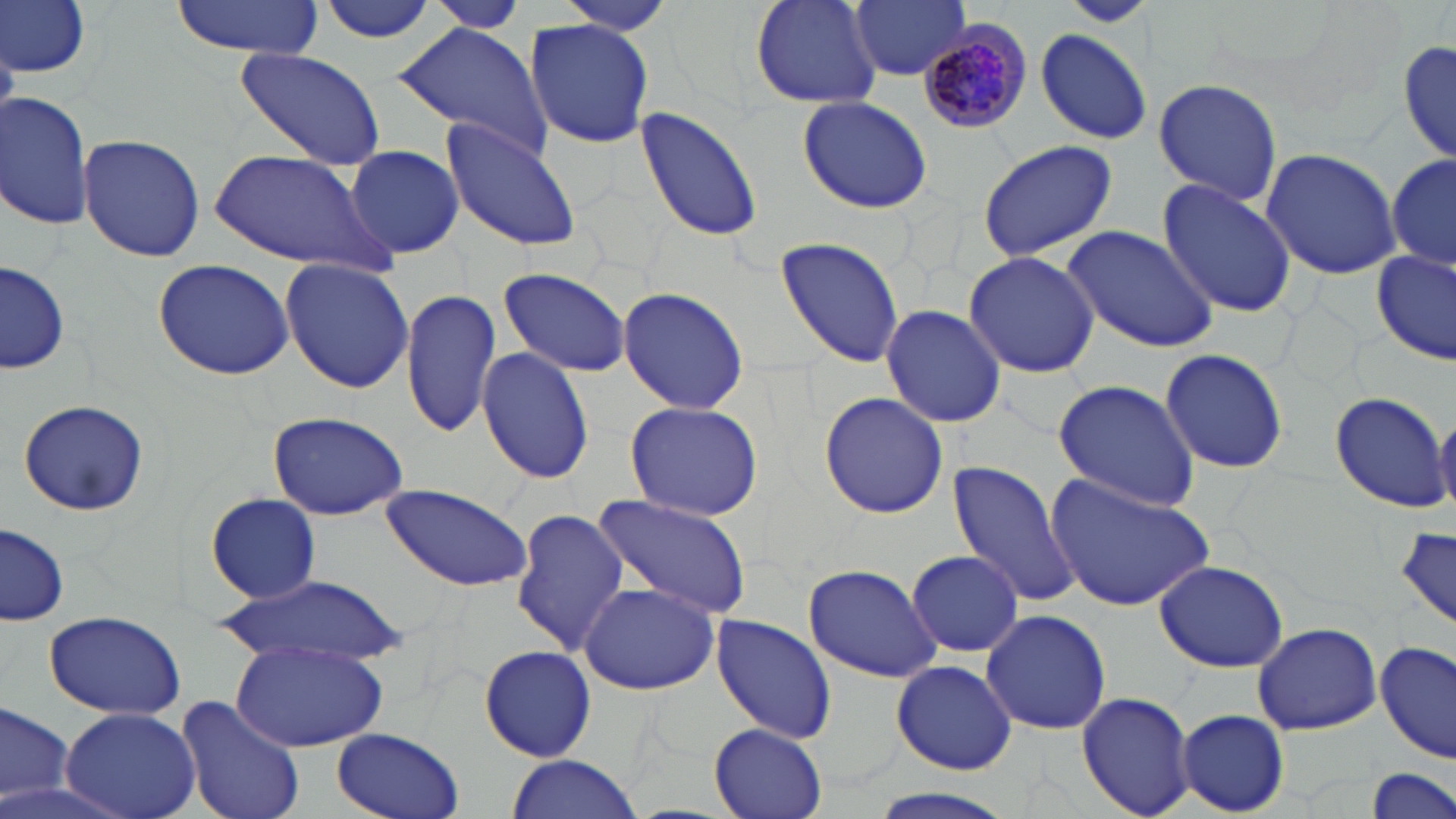
Summary:
  - Coordinate format: approximate bounding boxes as named x1/y1/x2/y2 corners in pixels
  - Uninfected red blood cell locations: (x1=1, y1=0, x2=91, y2=79), (x1=168, y1=0, x2=325, y2=58), (x1=316, y1=0, x2=443, y2=46), (x1=423, y1=0, x2=533, y2=32), (x1=553, y1=0, x2=677, y2=35), (x1=850, y1=0, x2=972, y2=81), (x1=1061, y1=0, x2=1154, y2=26), (x1=749, y1=1, x2=882, y2=108), (x1=523, y1=18, x2=657, y2=149), (x1=390, y1=21, x2=555, y2=163), (x1=1033, y1=27, x2=1153, y2=146), (x1=1396, y1=33, x2=1455, y2=170), (x1=232, y1=47, x2=386, y2=169), (x1=1154, y1=77, x2=1285, y2=207), (x1=1, y1=91, x2=95, y2=231), (x1=796, y1=95, x2=933, y2=213), (x1=636, y1=108, x2=765, y2=247), (x1=442, y1=121, x2=584, y2=249), (x1=77, y1=132, x2=205, y2=263), (x1=975, y1=137, x2=1122, y2=262), (x1=342, y1=144, x2=465, y2=259), (x1=1261, y1=147, x2=1401, y2=281), (x1=209, y1=148, x2=389, y2=276), (x1=1387, y1=148, x2=1455, y2=276), (x1=1157, y1=178, x2=1297, y2=319), (x1=1064, y1=225, x2=1219, y2=353), (x1=773, y1=234, x2=906, y2=367), (x1=1374, y1=249, x2=1455, y2=366), (x1=962, y1=250, x2=1101, y2=378), (x1=279, y1=257, x2=413, y2=394), (x1=1, y1=259, x2=70, y2=377), (x1=153, y1=259, x2=295, y2=380), (x1=499, y1=266, x2=629, y2=378), (x1=618, y1=284, x2=748, y2=416), (x1=402, y1=287, x2=501, y2=438), (x1=879, y1=304, x2=1006, y2=428), (x1=478, y1=346, x2=594, y2=485), (x1=1161, y1=347, x2=1289, y2=474), (x1=1051, y1=380, x2=1199, y2=511), (x1=1327, y1=388, x2=1450, y2=512), (x1=818, y1=392, x2=949, y2=519), (x1=17, y1=397, x2=150, y2=517), (x1=624, y1=400, x2=765, y2=522), (x1=267, y1=412, x2=409, y2=521), (x1=1432, y1=413, x2=1456, y2=513), (x1=948, y1=460, x2=1081, y2=606), (x1=1043, y1=471, x2=1215, y2=615), (x1=379, y1=483, x2=535, y2=594), (x1=204, y1=493, x2=320, y2=603), (x1=590, y1=493, x2=756, y2=623), (x1=510, y1=508, x2=629, y2=654), (x1=1, y1=522, x2=70, y2=625), (x1=1394, y1=527, x2=1456, y2=629), (x1=907, y1=549, x2=1025, y2=658), (x1=1154, y1=559, x2=1288, y2=673), (x1=801, y1=563, x2=942, y2=682), (x1=218, y1=577, x2=407, y2=668), (x1=576, y1=580, x2=720, y2=695), (x1=981, y1=608, x2=1111, y2=736), (x1=42, y1=610, x2=187, y2=719), (x1=709, y1=614, x2=839, y2=746), (x1=1250, y1=621, x2=1383, y2=736), (x1=232, y1=640, x2=389, y2=753), (x1=1376, y1=640, x2=1455, y2=766), (x1=478, y1=646, x2=598, y2=761), (x1=891, y1=659, x2=1019, y2=776), (x1=1077, y1=691, x2=1195, y2=819), (x1=175, y1=692, x2=306, y2=819), (x1=1, y1=700, x2=73, y2=808), (x1=61, y1=706, x2=200, y2=819), (x1=1176, y1=709, x2=1289, y2=816), (x1=707, y1=725, x2=828, y2=819), (x1=332, y1=728, x2=463, y2=819), (x1=503, y1=754, x2=645, y2=819), (x1=1366, y1=766, x2=1455, y2=819), (x1=859, y1=788, x2=1023, y2=819)
  - Plasmodium malariae-infected red blood cell locations: (x1=916, y1=25, x2=1033, y2=133)
  - Slide-level diagnosis: Plasmodium malariae
  - Magnification: 1000x
  - Stain: May-Grünwald-Giemsa
  - Modality: optical microscopy
  - Image size: 1456×819 pixels
  - Field of view: single
  - Preparation: thin blood smear